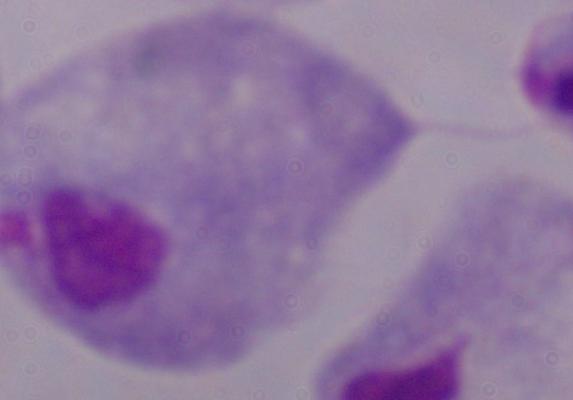
Summary:
  - Modality: micrograph
  - Magnification: 1000x
  - Identification: trichomonad